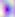

Summary:
  - Modality: photomicrograph
  - Identification: Toxoplasma gondii
  - Magnification: 400x